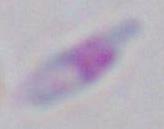

Toxoplasma gondii is shown. Captured at 1000x magnification. Micrograph.